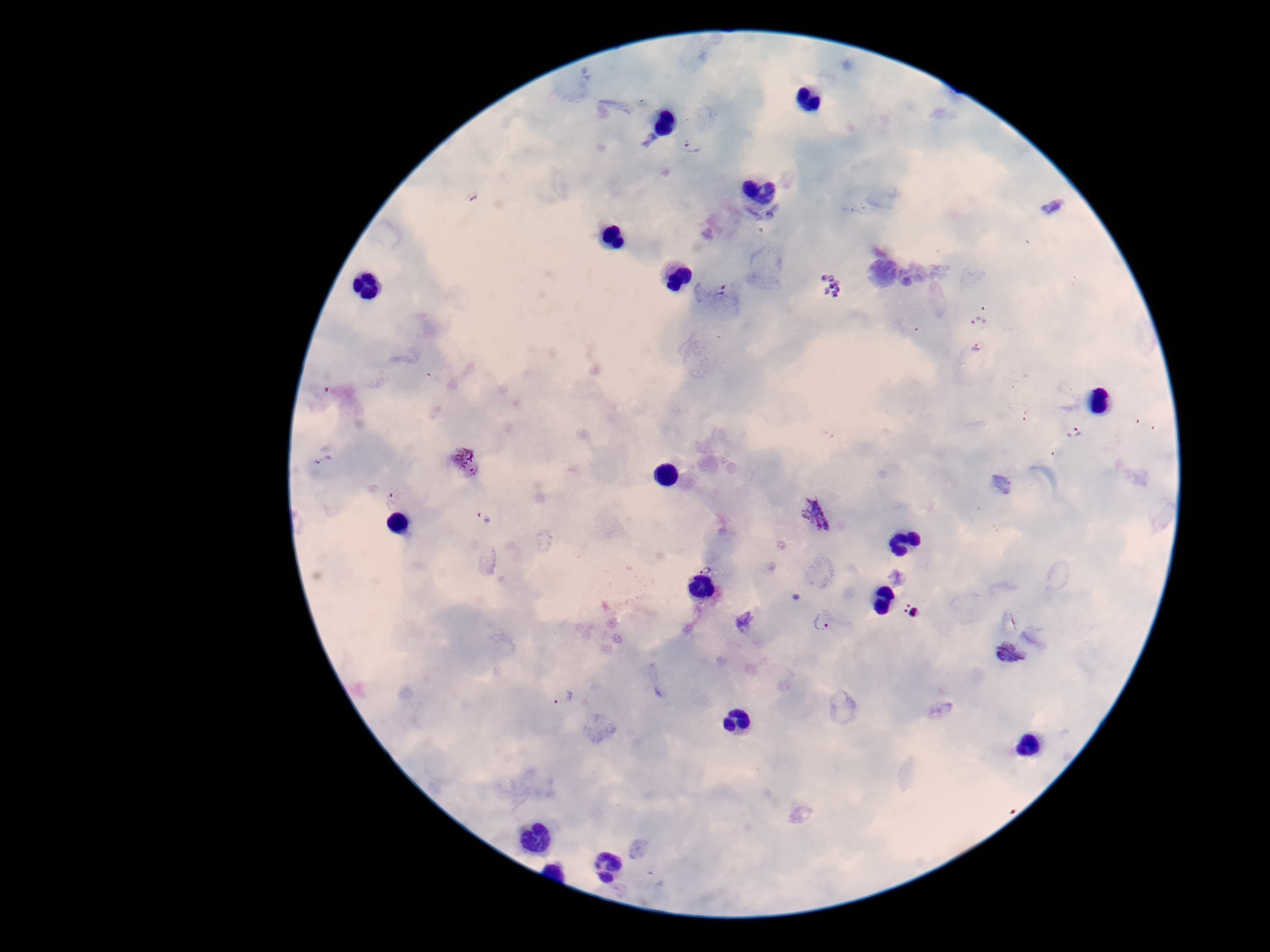
patient malaria status = positive
Plasmodium parasite locations = approximate centers as (x, y) in pixels: (692, 146), (1053, 207), (832, 284), (712, 291), (979, 320), (975, 349), (1075, 433), (466, 461), (389, 499), (818, 515), (483, 518), (707, 568), (911, 611), (744, 622), (822, 622), (1009, 653), (562, 697)
image size = 1270×952 pixels
stain = Giemsa
preparation = thick blood film
capture = smartphone camera through the microscope eyepiece
magnification = 100x
field of view = one from this slide